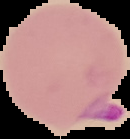

result = malaria parasites identified
image type = cell region segmented out of the field of view; surrounding area masked to black
preparation = thin blood smear
image size = 130×139 pixels